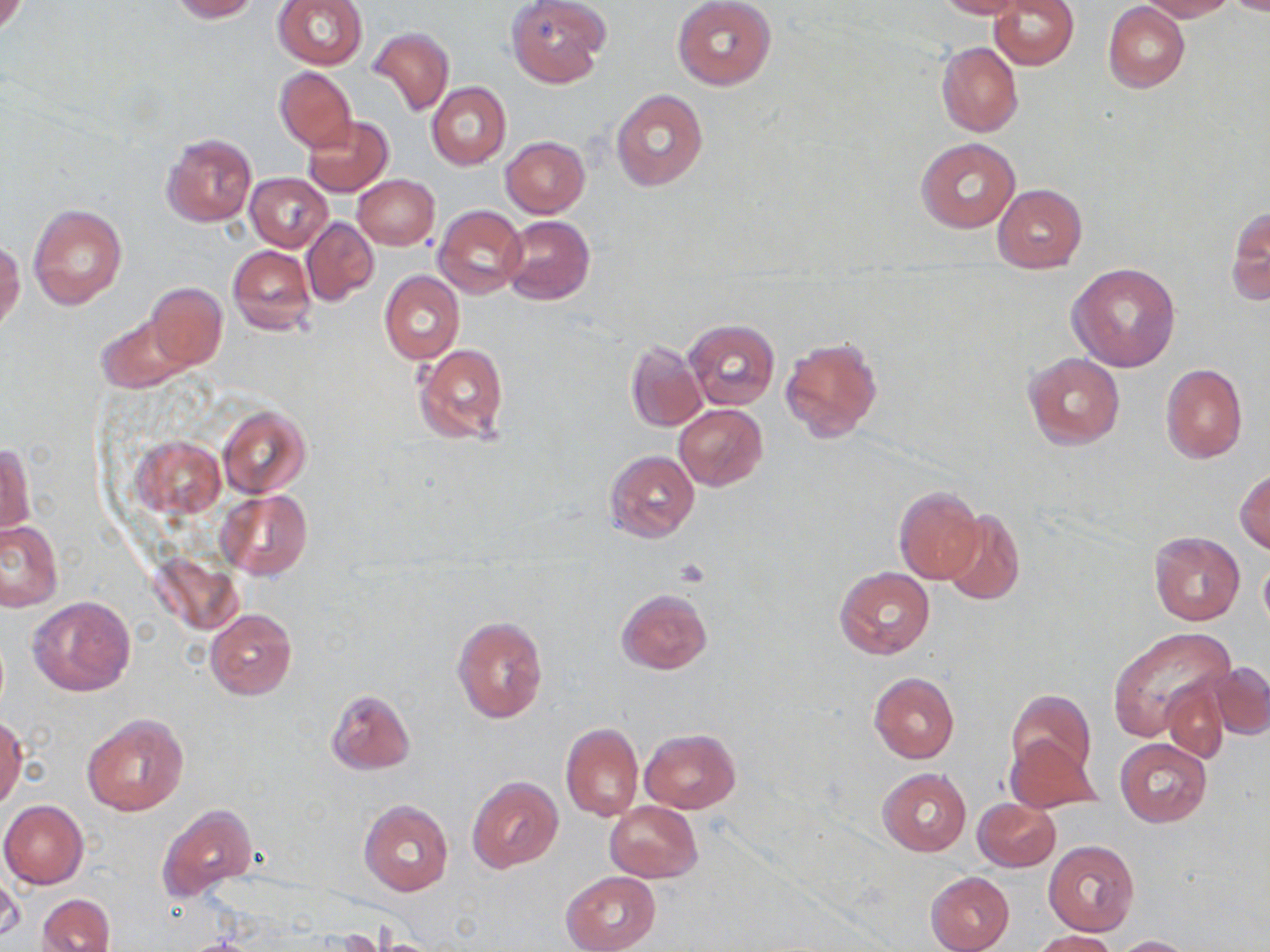

Summary:
  - Coordinate format: approximate bounding boxes as (x1,y1)-(x2,y2) corner pairs in pixels
  - Platelet locations: (675,559)-(710,589)
  - Uninfected red blood cell locations: (167,0)-(260,22), (506,0)-(608,87), (673,0)-(776,90), (935,0)-(1024,18), (989,0)-(1078,70), (1141,0)-(1234,21), (273,1)-(367,70), (1104,2)-(1190,92), (370,27)-(453,117), (936,41)-(1023,138), (275,67)-(357,150), (426,82)-(511,170), (611,89)-(708,191), (303,116)-(394,197), (161,132)-(256,228), (501,137)-(589,218), (916,138)-(1020,232), (247,173)-(332,251), (353,175)-(439,249), (992,183)-(1088,272), (29,202)-(127,309), (1227,203)-(1269,308), (434,205)-(527,298), (500,215)-(594,304), (302,218)-(379,306), (0,239)-(25,334), (228,245)-(315,336), (1067,262)-(1180,371), (379,271)-(464,365), (141,283)-(225,369), (94,310)-(203,393), (684,319)-(780,410), (780,334)-(885,444), (624,340)-(706,432), (413,342)-(509,445), (1024,352)-(1125,449), (1160,363)-(1248,464), (674,404)-(768,491), (217,405)-(310,498), (131,435)-(225,517), (1,441)-(34,540), (605,449)-(699,543), (1235,467)-(1270,555), (894,486)-(987,585), (216,490)-(313,581), (939,510)-(1025,607), (0,520)-(63,611), (1148,529)-(1245,626), (154,555)-(245,635), (1258,556)-(1270,634), (835,567)-(934,660), (616,588)-(711,675), (28,596)-(136,697), (205,608)-(296,700), (452,615)-(549,725), (1107,628)-(1234,740), (1206,661)-(1270,740), (869,672)-(960,763), (1162,675)-(1230,762), (1008,688)-(1097,778), (325,689)-(415,775), (82,713)-(189,818), (0,716)-(25,811), (560,722)-(643,822), (641,728)-(740,813), (1005,734)-(1100,815), (1115,739)-(1211,827), (877,768)-(971,857), (467,777)-(564,873), (974,798)-(1061,872), (359,799)-(454,896), (0,800)-(88,889), (605,802)-(701,882), (157,805)-(259,902), (1044,840)-(1139,935), (0,868)-(22,945), (561,871)-(661,952), (925,871)-(1014,952), (38,893)-(114,952), (1031,930)-(1117,951), (1114,936)-(1194,952)
  - Slide-level diagnosis: negative for blood parasites
  - Field of view: single
  - Magnification: 1000x
  - Image size: 1270×952 pixels
  - Modality: light microscopy
  - Preparation: thin blood smear
  - Stain: May-Grünwald-Giemsa